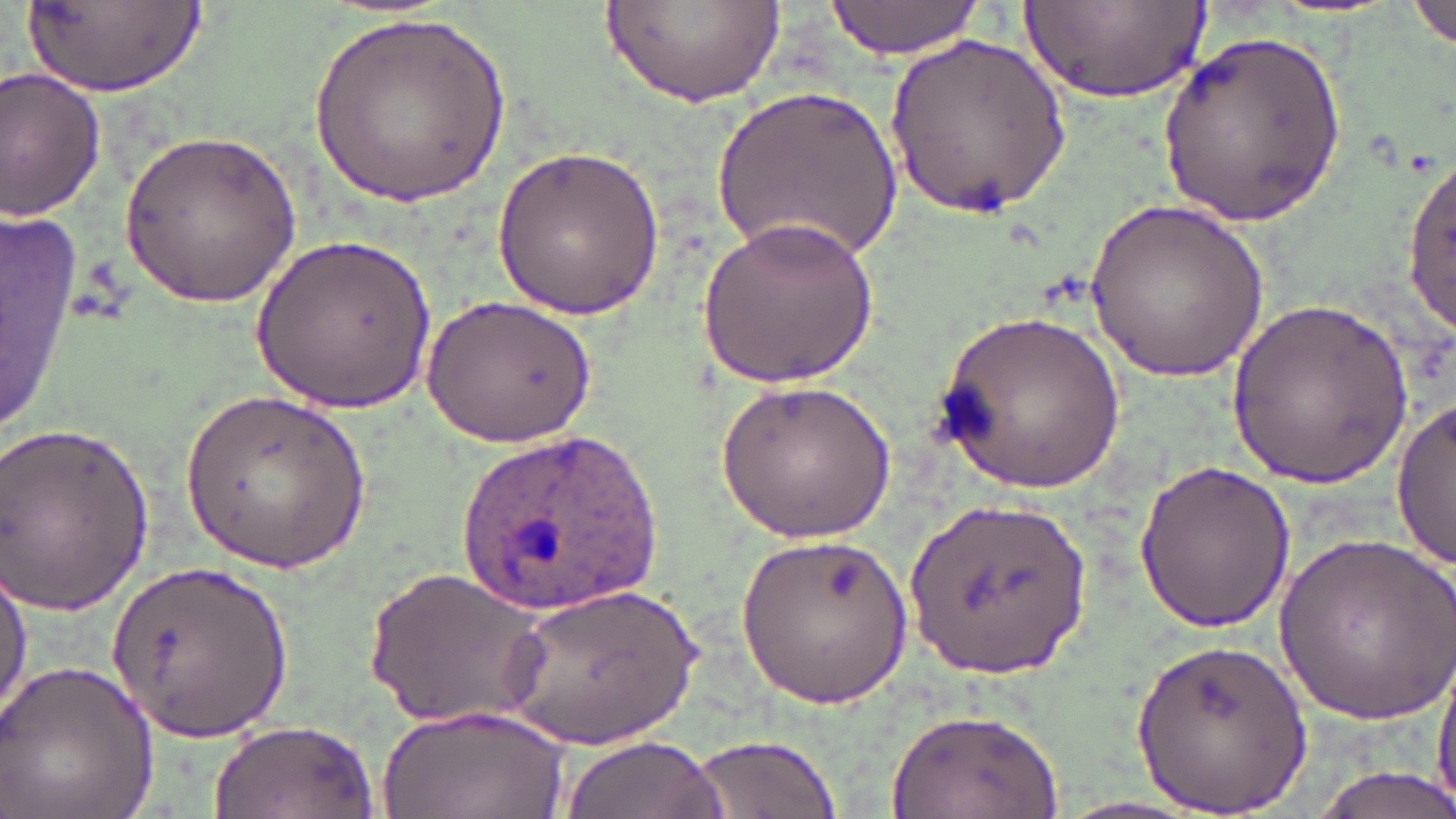
Summary:
  - Coordinate format: approximate bounding boxes as named x1/y1/x2/y2 corners in pixels
  - Plasmodium ovale-infected red blood cell locations: (x1=450, y1=431, x2=666, y2=608)
  - Uninfected red blood cell locations: (x1=605, y1=0, x2=784, y2=110), (x1=824, y1=0, x2=988, y2=61), (x1=1411, y1=1, x2=1456, y2=51), (x1=29, y1=2, x2=207, y2=99), (x1=1027, y1=3, x2=1211, y2=102), (x1=310, y1=8, x2=513, y2=208), (x1=1157, y1=30, x2=1347, y2=232), (x1=887, y1=36, x2=1073, y2=214), (x1=0, y1=70, x2=104, y2=221), (x1=715, y1=80, x2=900, y2=267), (x1=118, y1=129, x2=305, y2=306), (x1=491, y1=145, x2=670, y2=318), (x1=1403, y1=149, x2=1456, y2=339), (x1=1087, y1=199, x2=1273, y2=381), (x1=0, y1=207, x2=83, y2=442), (x1=699, y1=208, x2=879, y2=389), (x1=255, y1=231, x2=436, y2=415), (x1=423, y1=292, x2=598, y2=448), (x1=1229, y1=294, x2=1413, y2=489), (x1=937, y1=305, x2=1126, y2=493), (x1=714, y1=379, x2=895, y2=543), (x1=180, y1=388, x2=371, y2=575), (x1=1392, y1=399, x2=1455, y2=570), (x1=0, y1=417, x2=158, y2=613), (x1=1133, y1=459, x2=1295, y2=632), (x1=912, y1=494, x2=1094, y2=679), (x1=1274, y1=529, x2=1454, y2=719), (x1=738, y1=533, x2=914, y2=709), (x1=104, y1=557, x2=301, y2=747), (x1=1, y1=560, x2=32, y2=734), (x1=363, y1=566, x2=554, y2=732), (x1=500, y1=579, x2=708, y2=747), (x1=1130, y1=638, x2=1313, y2=814), (x1=1434, y1=653, x2=1456, y2=810), (x1=0, y1=658, x2=160, y2=819), (x1=378, y1=703, x2=571, y2=819), (x1=884, y1=708, x2=1064, y2=819), (x1=202, y1=718, x2=381, y2=819), (x1=561, y1=733, x2=730, y2=819), (x1=686, y1=734, x2=845, y2=819), (x1=1305, y1=766, x2=1456, y2=819)
  - Slide-level diagnosis: Plasmodium ovale
  - Modality: optical microscopy
  - Stain: May-Grünwald-Giemsa
  - Image size: 1456×819 pixels
  - Preparation: thin blood smear
  - Magnification: 1000x
  - Field of view: single